Classify this cell by malaria status.
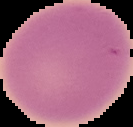

It is uninfected.

From a thin blood smear. Image is 133×127 pixels. Segmented cell region on a black background.